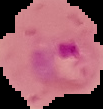

malaria status = parasitized
image type = segmented cell region on a black background
image size = 103×109 pixels
preparation = thin blood film